Classify this cell by malaria status.
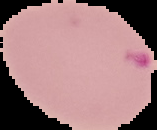
It is parasitized.

Summary:
  - Image type: cell region segmented out of the field of view; surrounding area masked to black
  - Image size: 157×130 pixels
  - Preparation: thin blood film